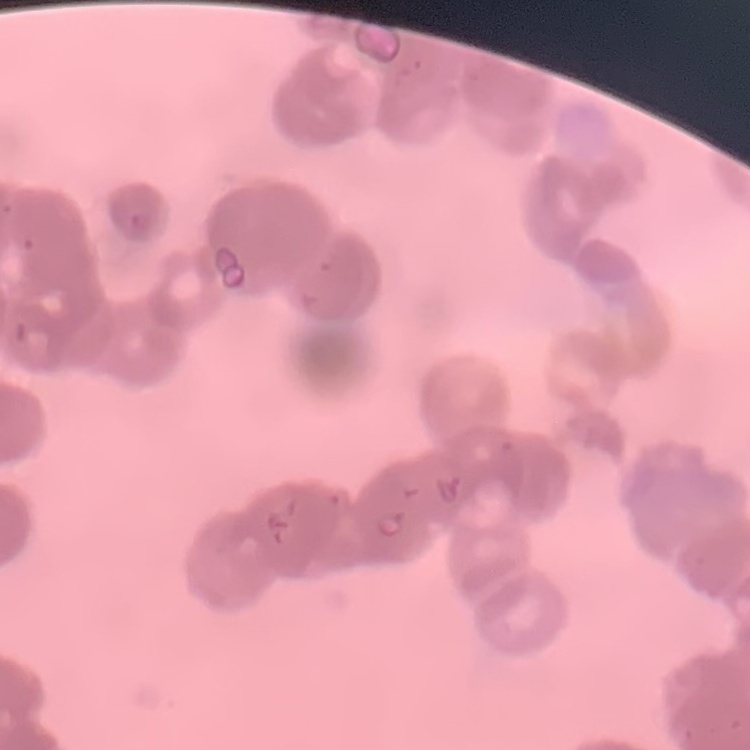

erythrocyte morphology = rouleaux formation
preparation = thin peripheral smear
stain = Field's or Giemsa
image type = one tile cut from a larger photomicrograph